Locate every malaria parasite.
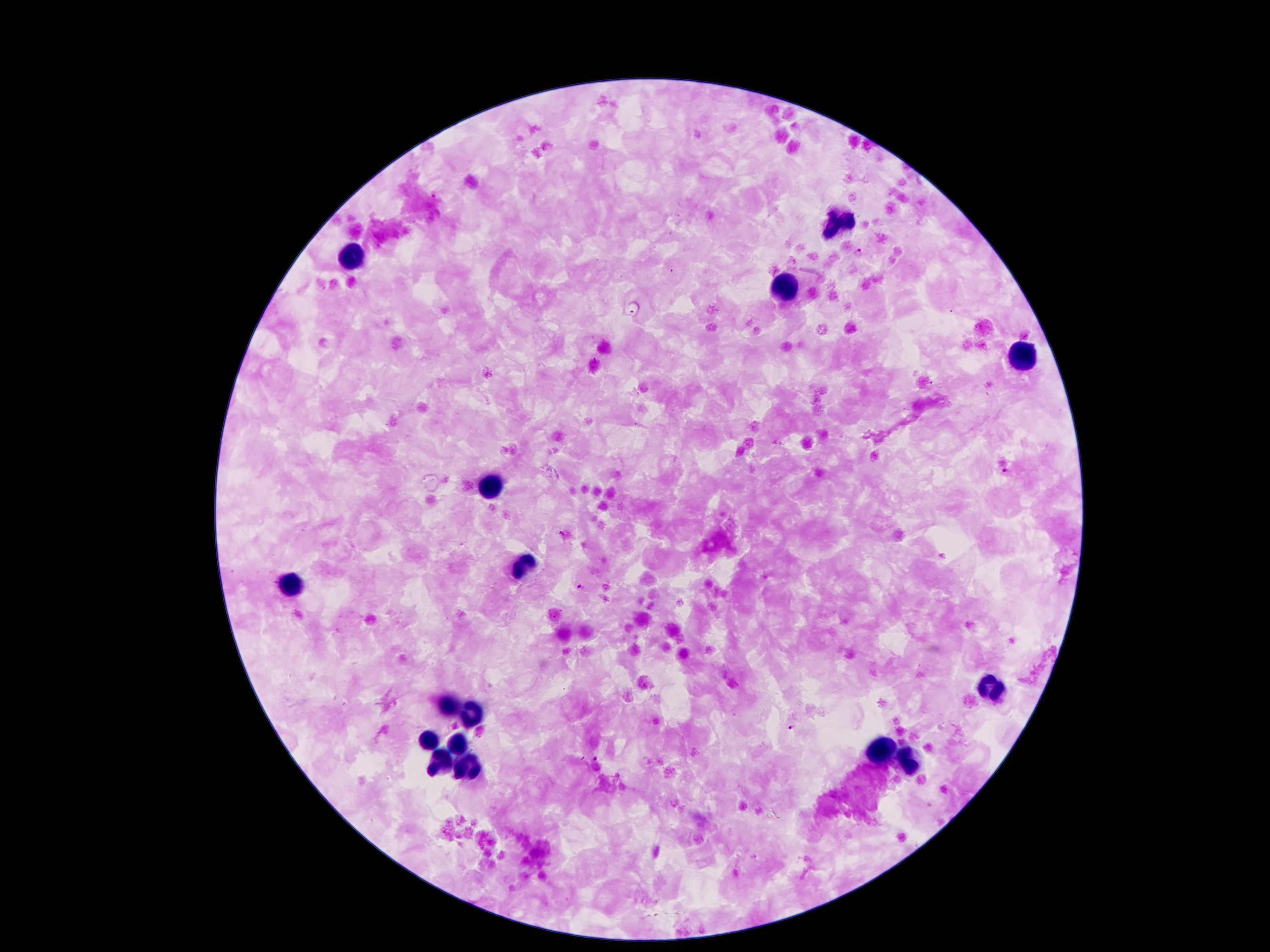

Approximate centers as [x, y] in pixels.
Malaria parasites: [858, 251], [631, 311], [1005, 471], [581, 588], [794, 728], [595, 759].

preparation: thick peripheral-blood smear
image_size: 1270×952 pixels
field_of_view: single
leukocyte_locations: 'approximate centers as [x, y] in pixels: [839, 220], [354, 257], [783, 289], [1018, 356], [489, 480], [526, 566], [287, 585], [993, 692], [447, 704], [470, 715], [428, 742], [459, 746], [881, 751], [444, 761], [911, 761], [468, 767]'
magnification: 100x
capture: smartphone through the microscope eyepiece
stain: Giemsa
patient_malaria_status: positive for Plasmodium falciparum